Locate and identify every blood parasite.
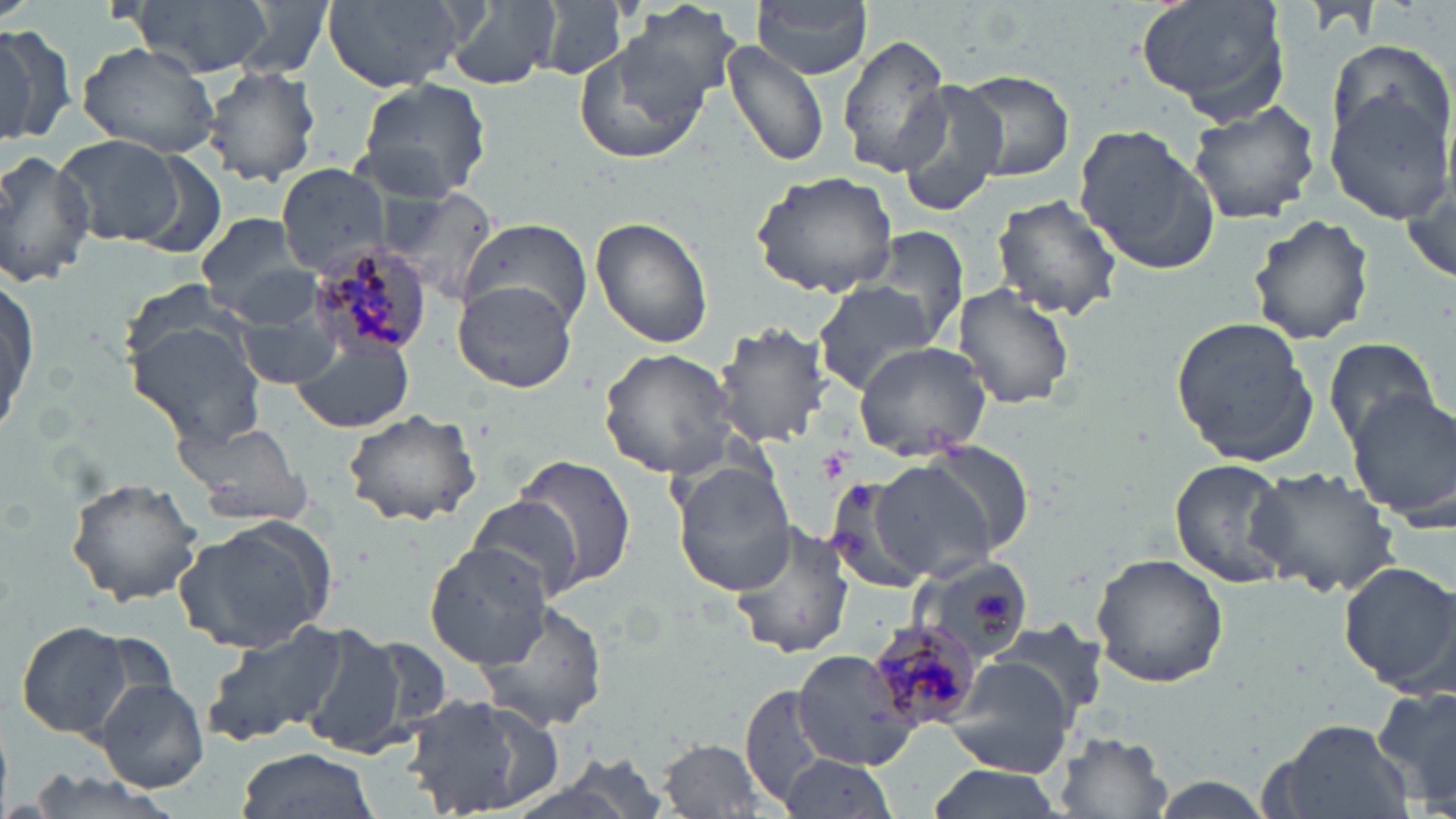
Approximate bounding boxes as (x1,y1)-(x2,y2) corner pairs in pixels.
Plasmodium malariae-infected red blood cells: (310,245)-(434,357), (861,623)-(978,732).
No Plasmodium falciparum, Plasmodium ovale, Plasmodium vivax, Babesia divergens, or Trypanosoma brucei observed.

{
  "slide_level_diagnosis": "Plasmodium malariae",
  "image_size": "1456×819 pixels",
  "modality": "light microscopy",
  "magnification": "1000x",
  "preparation": "thin blood smear",
  "field_of_view": "one of a larger specimen",
  "uninfected_red_blood_cell_locations": "approximate bounding boxes as (x1,y1)-(x2,y2) corner pairs in pixels: (126,0)-(272,78), (233,0)-(333,77), (320,0)-(474,93), (537,0)-(628,82), (753,0)-(873,79), (1132,0)-(1293,122), (444,1)-(557,90), (616,2)-(744,112), (0,23)-(77,147), (838,34)-(953,178), (721,40)-(828,169), (1327,41)-(1455,157), (77,42)-(220,159), (573,42)-(708,165), (202,65)-(321,187), (943,69)-(1078,184), (1324,77)-(1456,218), (354,78)-(493,203), (896,82)-(1011,213), (1187,99)-(1322,224), (1071,121)-(1220,277), (54,135)-(188,248), (0,147)-(97,288), (276,161)-(393,276), (1399,162)-(1455,292), (752,169)-(903,298), (382,190)-(504,301), (990,194)-(1123,322), (193,212)-(315,317), (1247,212)-(1375,346), (591,215)-(714,348), (460,219)-(591,333), (872,227)-(969,352), (2,268)-(38,443), (811,279)-(939,393), (453,280)-(577,393), (952,285)-(1076,410), (233,306)-(348,387), (1171,316)-(1319,465), (125,320)-(265,451), (717,321)-(834,446), (291,335)-(414,434), (1321,335)-(1446,453), (852,340)-(994,462), (598,348)-(738,478), (1348,388)-(1456,531), (342,408)-(482,528), (175,418)-(310,528), (914,442)-(1034,561), (516,454)-(638,587), (867,457)-(1004,583), (1169,458)-(1297,590), (672,461)-(800,595), (1246,463)-(1399,598), (65,476)-(205,610), (825,476)-(937,595), (463,494)-(586,604), (174,515)-(338,654), (729,521)-(854,659), (424,544)-(553,668), (1089,550)-(1231,689), (910,554)-(1034,659), (1339,561)-(1456,695), (474,599)-(608,733), (13,620)-(140,741), (202,621)-(348,747), (987,621)-(1106,720), (292,628)-(436,762), (791,649)-(923,771), (942,656)-(1075,776), (94,677)-(209,793), (1375,683)-(1456,812), (741,686)-(832,805), (396,690)-(569,816), (1266,720)-(1416,819), (1055,732)-(1174,818), (660,738)-(773,816), (235,749)-(377,819), (777,754)-(901,819), (923,764)-(1064,819)",
  "stain": "May-Grünwald-Giemsa"
}